Classify this cell by malaria status.
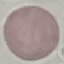

Uninfected.

Giemsa-stained preparation. Thin blood smear. Cell patch, automatically extracted from a larger field of view and resized to 64 × 64 pixels. Photographed with a smartphone camera at the microscope eyepiece.